Assess this cell for malaria.
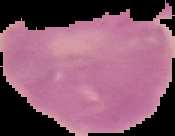
It is uninfected.

Summary:
  - Image size: 175×136 pixels
  - Preparation: thin blood film
  - Image type: cell region segmented out of the field of view; surrounding area masked to black